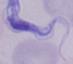

magnification = 1000x
modality = photomicrograph
identification = trypanosome